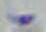

Summary:
  - Magnification: 1000x
  - Modality: micrograph
  - Identification: Toxoplasma gondii